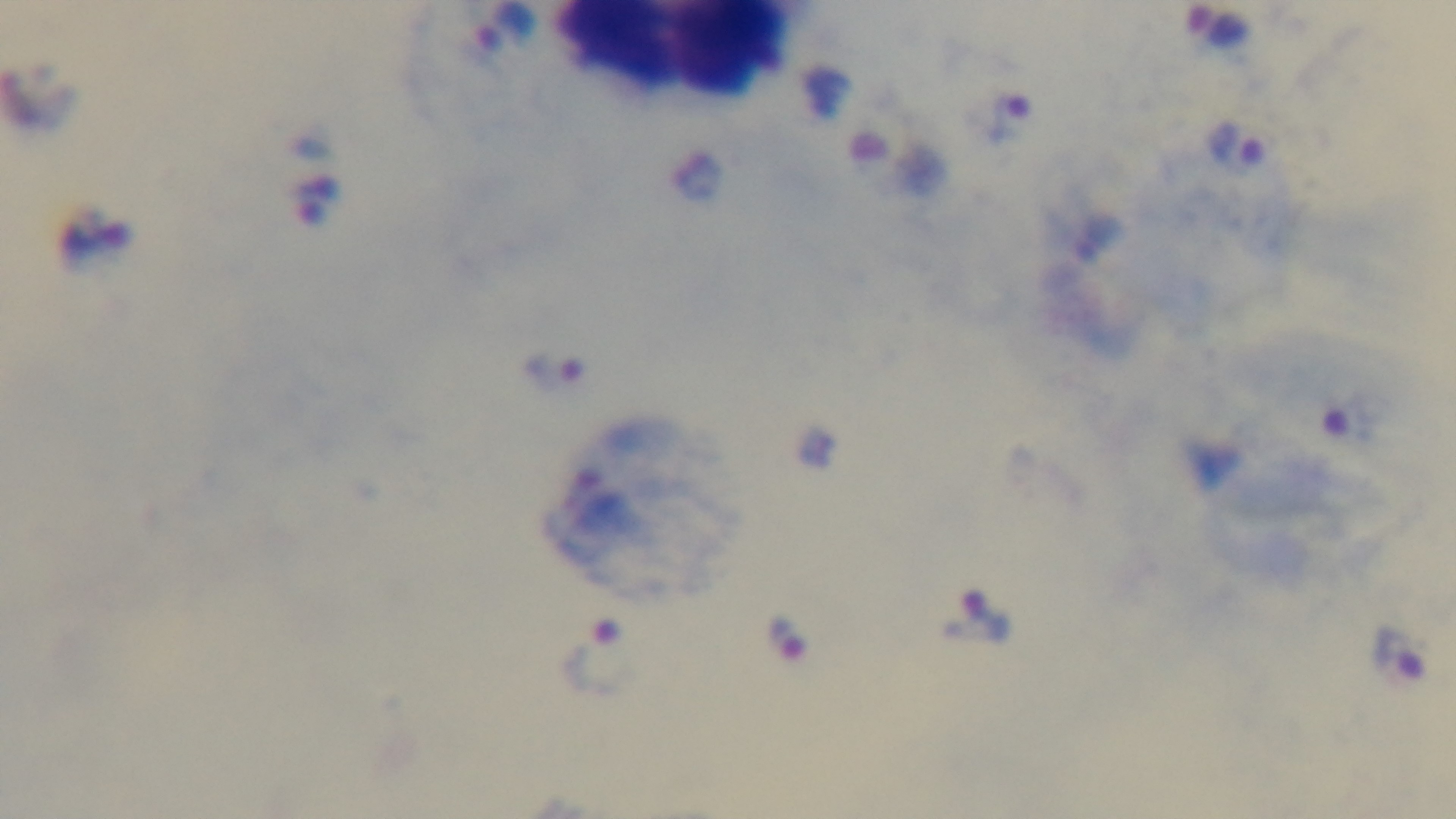

capture = mounted 4K digital camera
preparation = thick smear
modality = light microscopy
objective = 100x oil immersion
malaria status = infected
stain = Giemsa
field of view = one from the slide